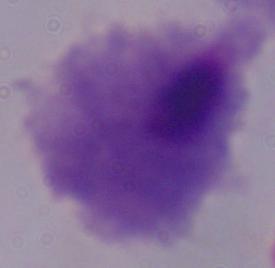

Summary:
  - Identification: trichomonad
  - Modality: micrograph
  - Magnification: 1000x